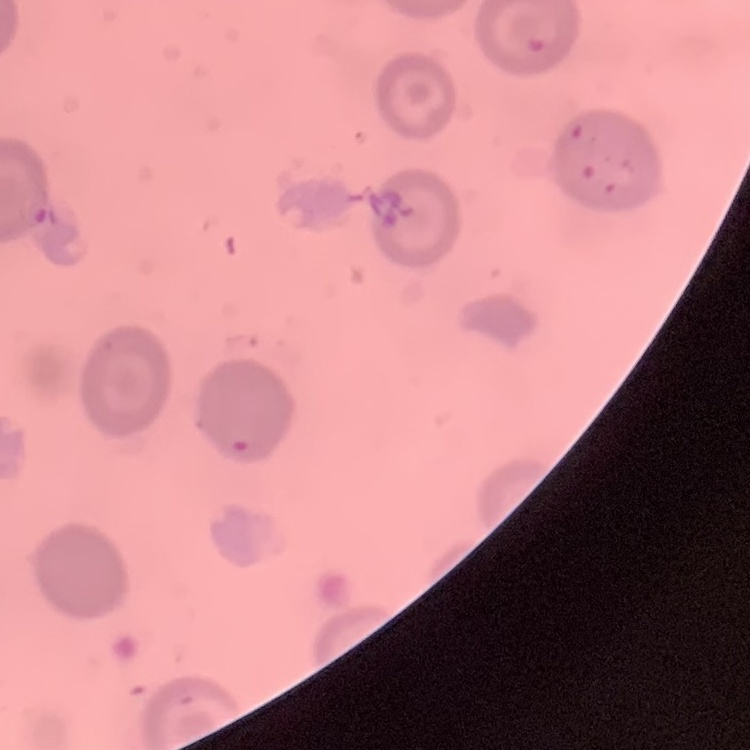

erythrocyte_morphology: no rouleaux formation
stain: Field's or Giemsa
preparation: thin blood smear
image_type: one tile cut from a larger photomicrograph